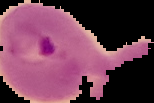
result = malaria parasites detected
image type = segmented cell region on a black background
image size = 154×103 pixels
preparation = thin blood smear